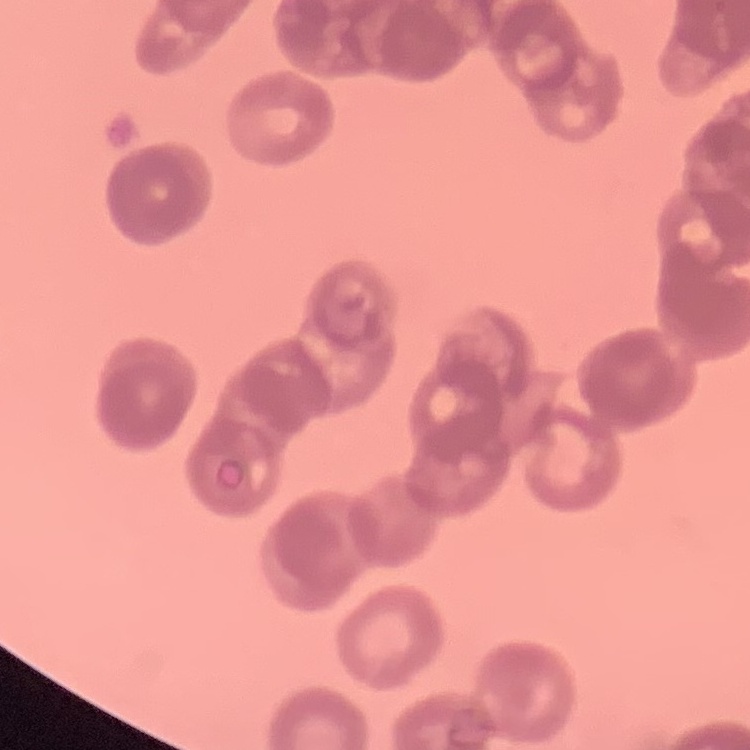

The red blood cells show rouleaux formation. Square crop of a larger photomicrograph. Thin blood film. Field's or Giemsa stain.